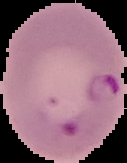
{
  "image_type": "cell region segmented out of the field of view; surrounding area masked to black",
  "preparation": "thin blood film",
  "image_size": "127×163 pixels",
  "malaria_status": "parasitized"
}